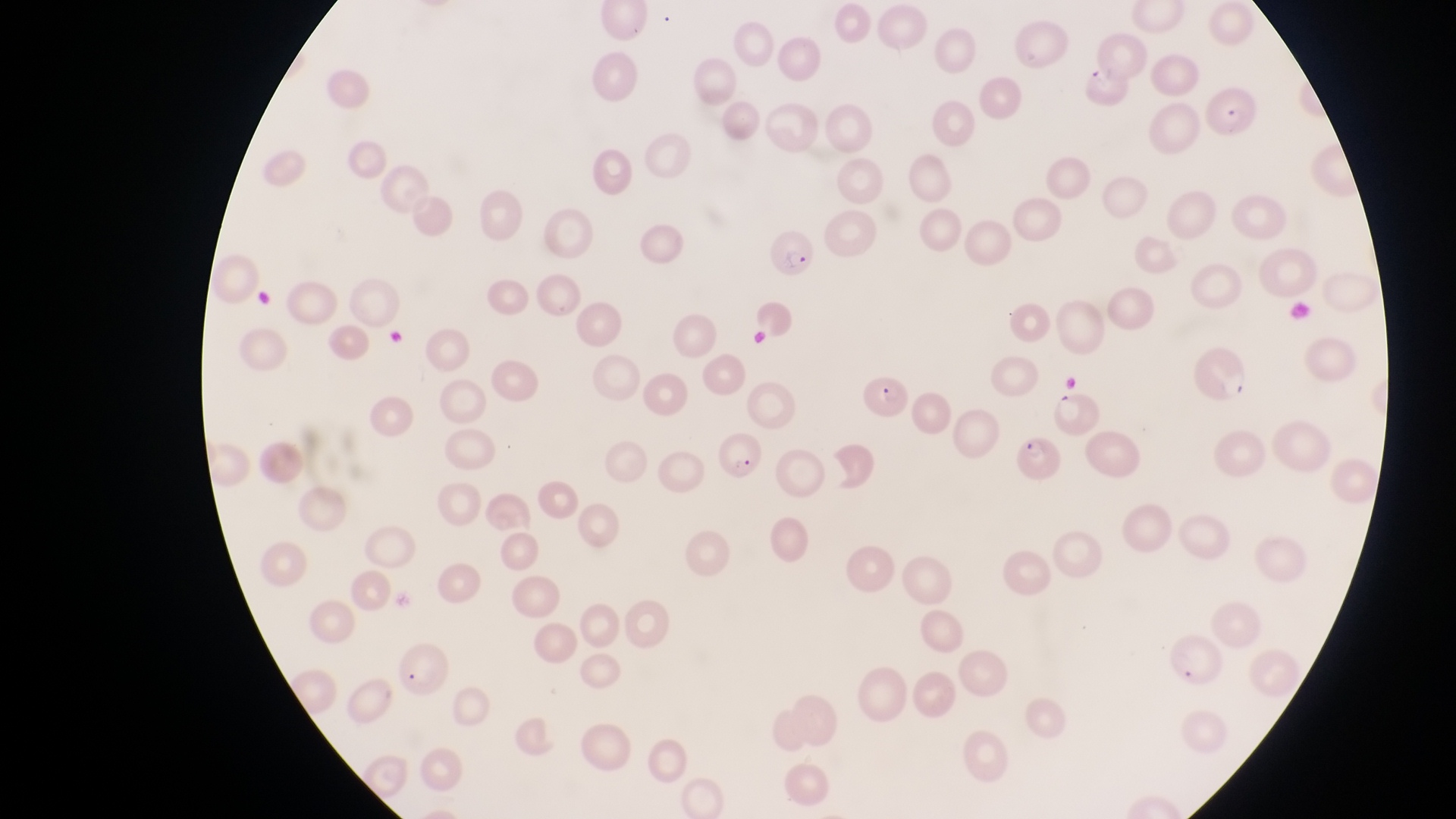

magnification = 1000x
image size = 1456×819 pixels
parasitised red blood cell locations = approximate bounding boxes as left top right bottom in pixels: 1084 61 1133 111; 1198 80 1259 138; 770 235 820 282; 854 372 909 422; 1050 394 1100 437; 708 430 767 485; 1015 430 1060 489
capture = smartphone photograph through the eyepiece of an Olympus CX-23 microscope
country = Uganda
preparation = thin blood film
field of view = single